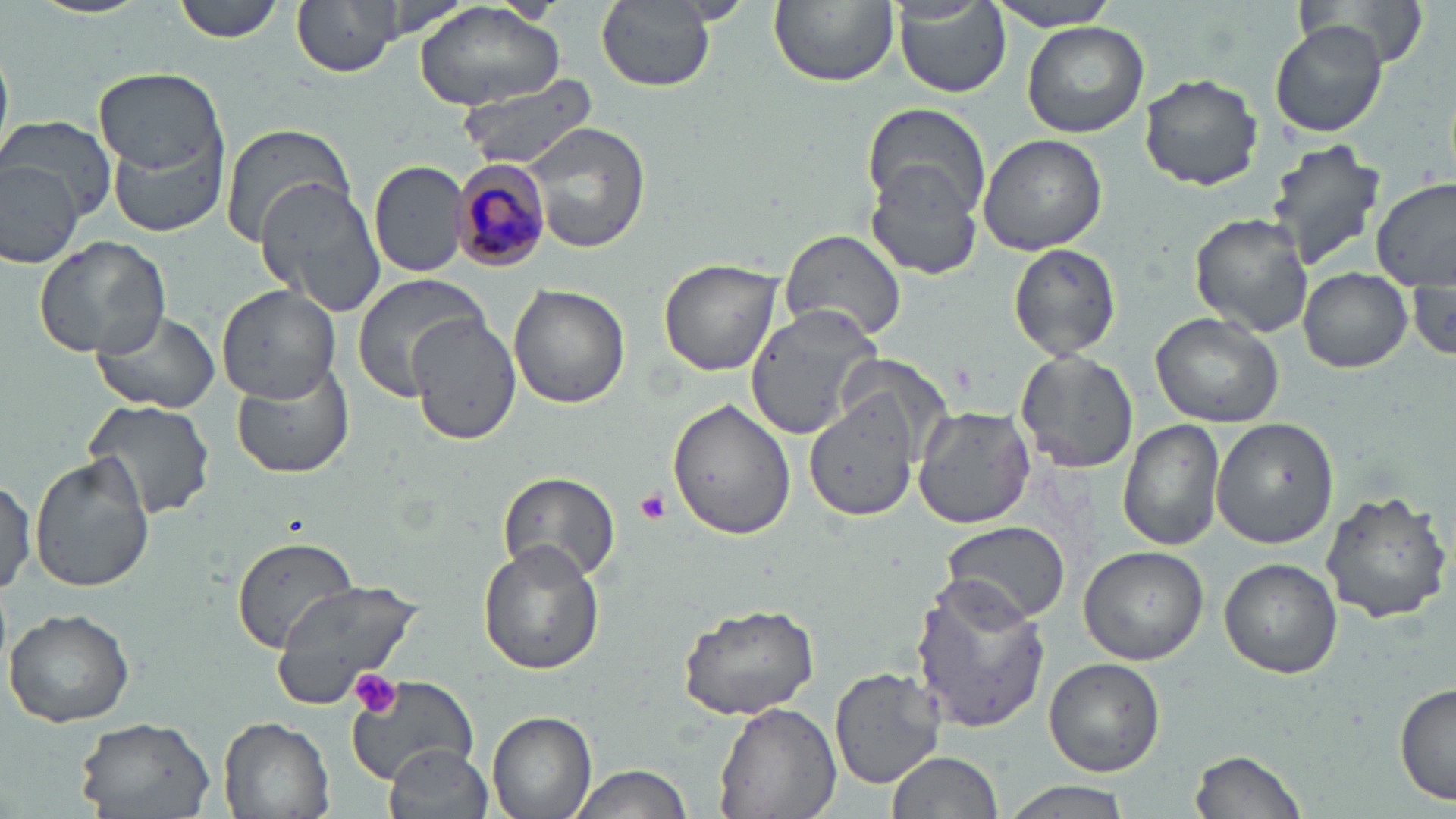

{
  "slide_level_diagnosis": "Plasmodium malariae",
  "modality": "optical microscopy",
  "image_size": "1456×819 pixels",
  "plasmodium_malariae_infected_red_blood_cell_locations": "approximate bounding boxes as (x1,y1)-(x2,y2) corner pairs in pixels: (448,161)-(552,272)",
  "uninfected_red_blood_cell_locations": "approximate bounding boxes as (x1,y1)-(x2,y2) corner pairs in pixels: (173,0)-(288,43), (294,0)-(402,78), (360,0)-(478,42), (593,0)-(719,95), (768,0)-(899,87), (1300,0)-(1431,72), (982,1)-(1125,31), (415,3)-(566,111), (893,3)-(1011,99), (1023,22)-(1148,137), (1270,22)-(1389,138), (94,69)-(227,176), (1139,72)-(1264,191), (455,78)-(603,169), (862,105)-(991,219), (5,118)-(117,225), (220,122)-(353,245), (525,123)-(650,253), (111,133)-(231,237), (978,134)-(1108,255), (1264,139)-(1387,269), (0,157)-(82,265), (369,160)-(472,277), (865,165)-(983,280), (1373,179)-(1456,294), (256,180)-(387,316), (1189,213)-(1313,336), (780,228)-(906,346), (32,235)-(170,359), (1008,244)-(1121,360), (659,255)-(782,376), (1409,265)-(1456,368), (1297,267)-(1412,373), (350,274)-(491,397), (217,285)-(341,402), (510,285)-(630,409), (742,303)-(884,440), (90,308)-(221,414), (397,308)-(522,445), (1150,310)-(1284,428), (1015,350)-(1138,472), (231,361)-(355,480), (805,392)-(919,521), (80,397)-(219,521), (668,397)-(796,541), (913,405)-(1035,528), (1118,419)-(1225,553), (1211,419)-(1338,549), (30,453)-(154,593), (495,472)-(622,585), (0,473)-(35,600), (1320,488)-(1452,623), (942,521)-(1069,624), (230,536)-(368,654), (478,541)-(604,674), (1078,544)-(1208,664), (1219,558)-(1343,679), (909,575)-(1052,732), (271,579)-(433,701), (678,601)-(822,720), (3,607)-(136,728), (1043,657)-(1166,776), (830,664)-(947,789), (346,674)-(480,785), (1394,684)-(1455,806), (711,699)-(841,819), (488,711)-(596,819), (219,715)-(337,819), (70,718)-(218,817), (385,745)-(495,819), (1188,747)-(1309,819), (885,750)-(1005,819), (565,763)-(699,819), (1001,780)-(1136,819)",
  "field_of_view": "one of a larger specimen",
  "preparation": "thin blood smear",
  "platelet_locations": "approximate bounding boxes as (x1,y1)-(x2,y2) corner pairs in pixels: (634,487)-(670,523), (351,670)-(403,719)",
  "stain": "May-Grünwald-Giemsa",
  "magnification": "1000x"
}